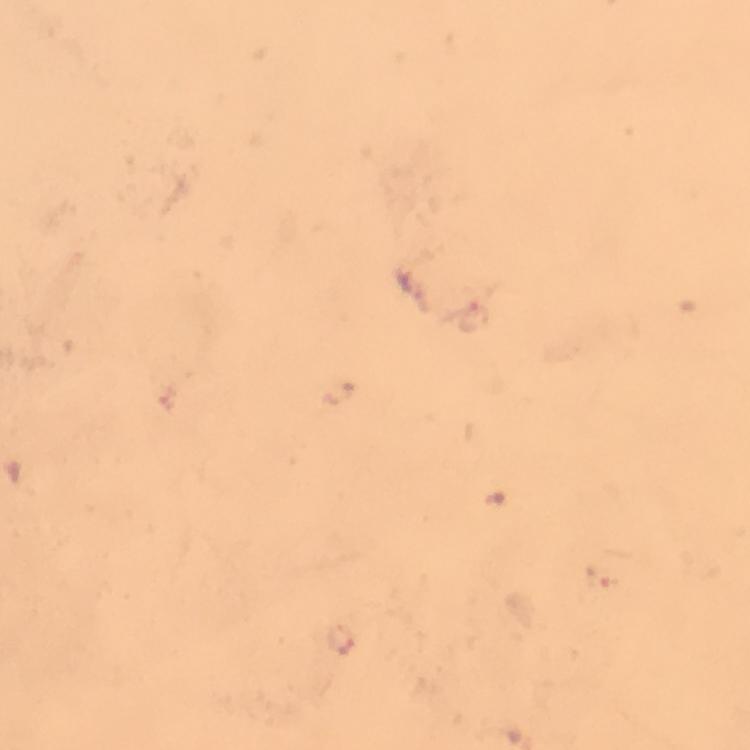
image_size: 750×750 pixels
preparation: thick smear
capture: smartphone photograph through a microscope
immersion_oil: applied
stain: Giemsa
magnification: 100x
cropped_from: a single field of view
malaria_parasite_locations: 'approximate centers as {x, y} in pixels: {475, 316}, {342, 638}'
context: from a diagnostic examination for malaria